Locate every malaria parasite.
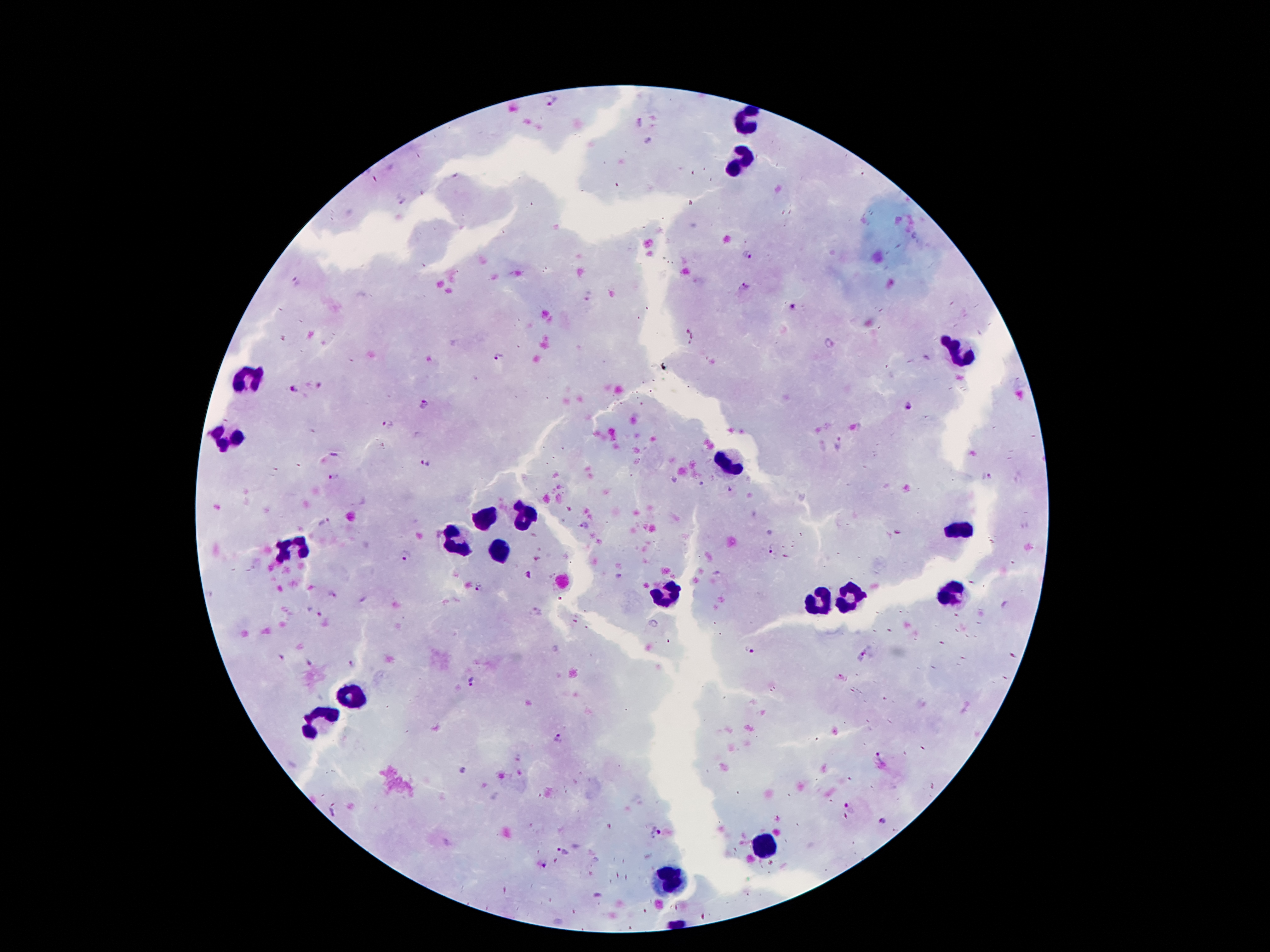
Approximate centers as {x, y} in pixels.
Malaria parasites: {550, 101}, {746, 254}, {297, 283}, {745, 286}, {793, 308}, {829, 343}, {499, 359}, {294, 389}, {426, 405}, {906, 405}, {388, 423}, {838, 442}, {425, 463}, {334, 477}, {989, 477}, {325, 522}, {773, 553}, {405, 555}, {479, 588}, {332, 594}, {317, 612}, {750, 650}, {862, 655}, {282, 658}, {309, 662}, {353, 662}, {473, 681}, {559, 739}, {882, 758}, {851, 806}, {334, 813}, {883, 822}, {656, 831}, {563, 851}.

Leukocyte locations: {747, 124}, {743, 158}, {956, 353}, {251, 382}, {227, 435}, {729, 464}, {526, 515}, {485, 519}, {963, 529}, {458, 539}, {294, 550}, {497, 552}, {954, 591}, {665, 597}, {848, 599}, {817, 603}, {356, 693}, {321, 722}, {762, 845}, {669, 886}. Smartphone photograph taken through the microscope eyepiece. Thick blood smear. Giemsa-stained preparation. Patient malaria status: infected with Plasmodium falciparum. 100x magnification. Image is 1270×952 pixels. One field from this slide.